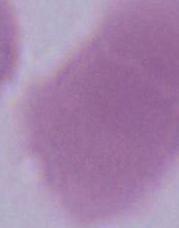
Captured at 1000x magnification. Photomicrograph. A red blood cell is seen.